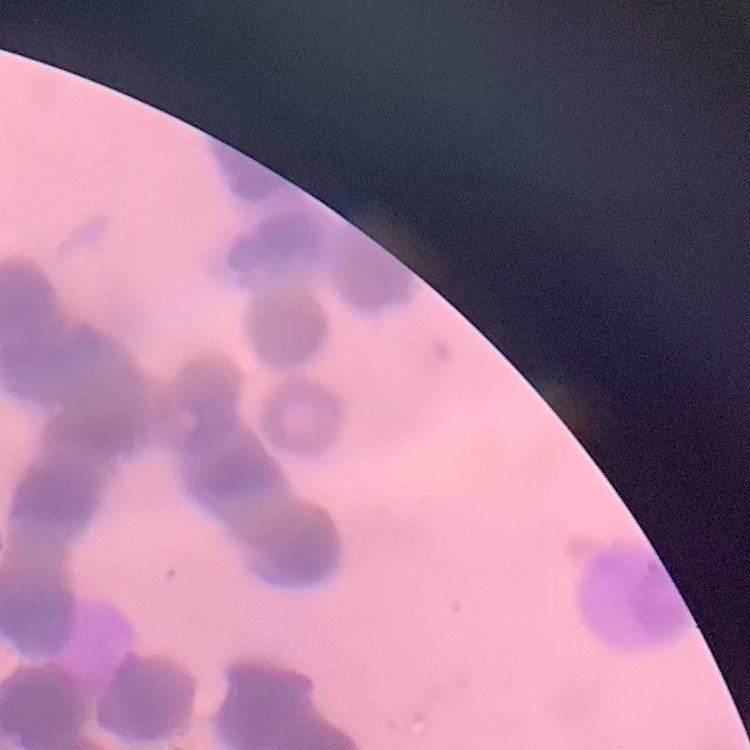

erythrocyte morphology = rouleaux formation
image type = one tile cut from a larger photomicrograph
stain = Field's or Giemsa
preparation = thin blood smear